State which parasite is depicted.
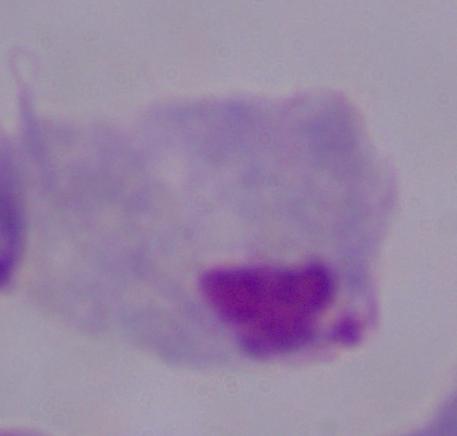
A trichomonad.

1000x magnification. Photomicrograph.